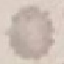

Result: negative for malaria parasites. Thin blood smear. Giemsa-stained preparation. Photographed with a smartphone camera at the microscope eyepiece. Automatically extracted cell patch, resized to 64 × 64 pixels.